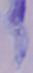
Summary:
  - Modality: photomicrograph
  - Identification: trypanosome
  - Magnification: 1000x